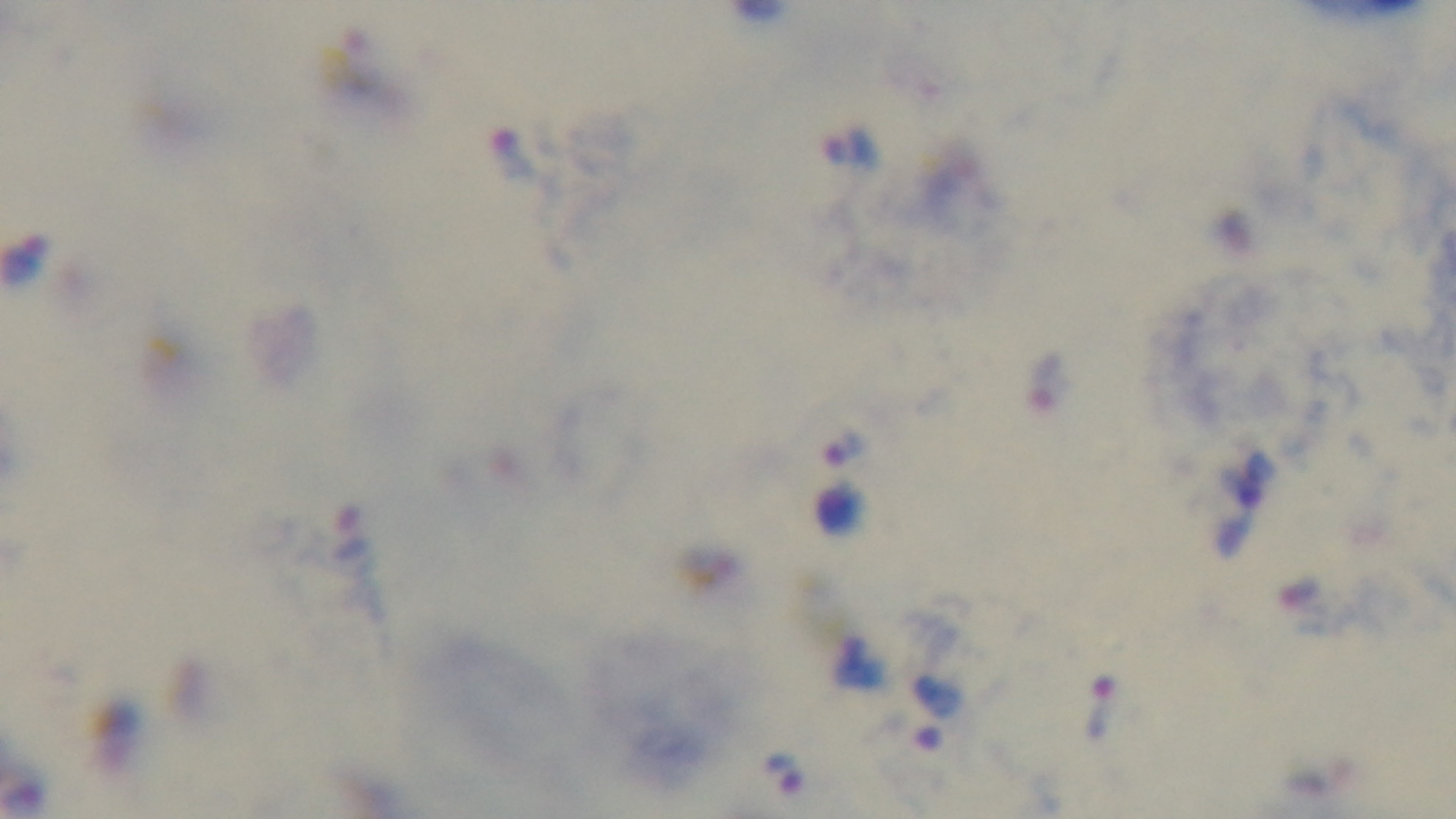

{
  "capture": "mounted 4K digital camera",
  "malaria_status": "positive",
  "preparation": "thick blood film",
  "objective": "100x oil immersion",
  "stain": "Giemsa",
  "field_of_view": "one from the slide",
  "modality": "light microscopy"
}